State the preparation type.
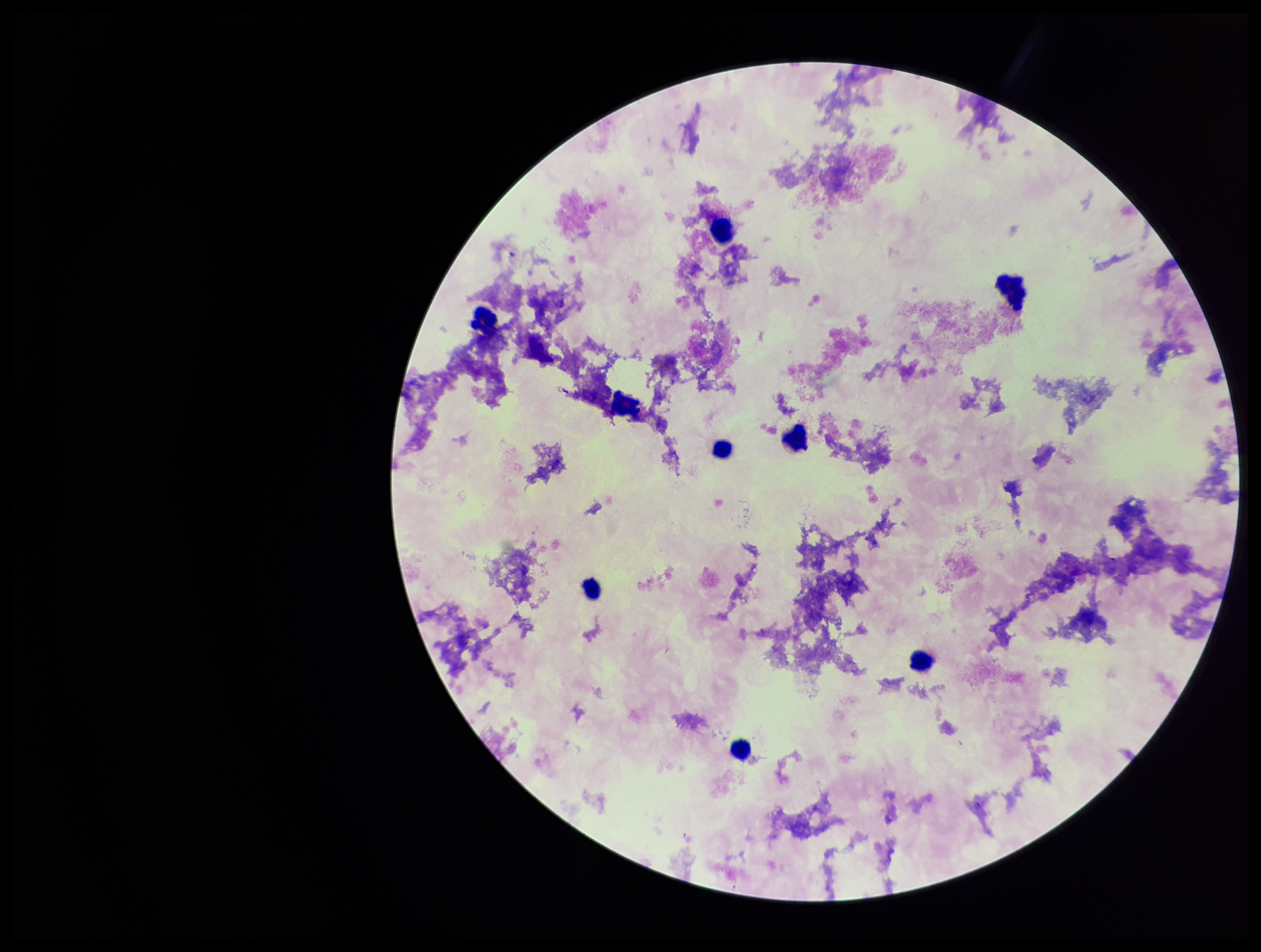

Thick.

field of view = single
stain = Giemsa
patient malaria status = negative
image size = 1261×952 pixels
capture = smartphone photograph through the microscope eyepiece
leukocyte count = 9
Plasmodium parasites = none seen
parasite count = 0